Name the cell type shown.
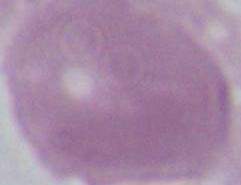
An erythrocyte.

Captured at 1000x magnification. Photomicrograph.